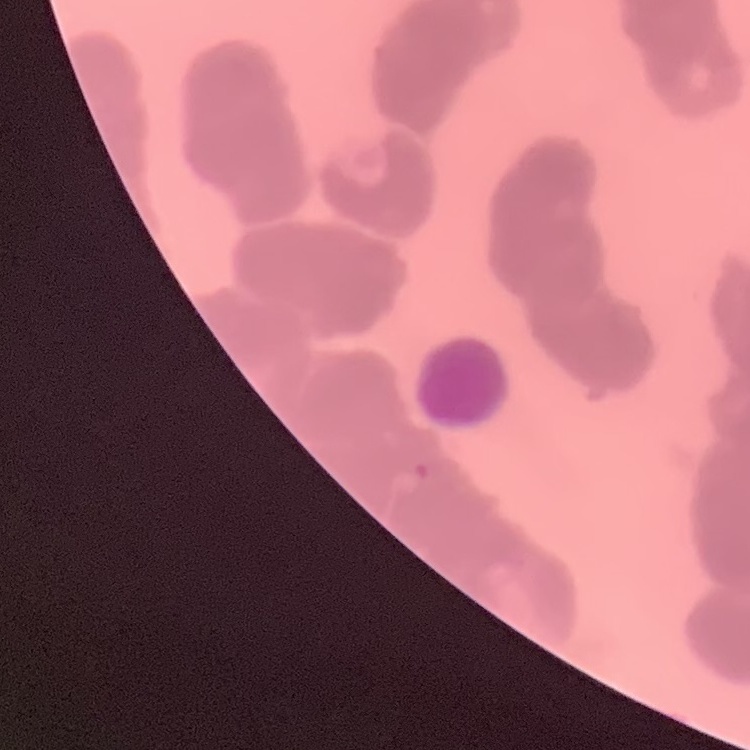
Summary:
  - Erythrocyte morphology: rouleaux formation
  - Stain: Field's or Giemsa
  - Preparation: thin blood smear
  - Image type: square crop of a larger photomicrograph